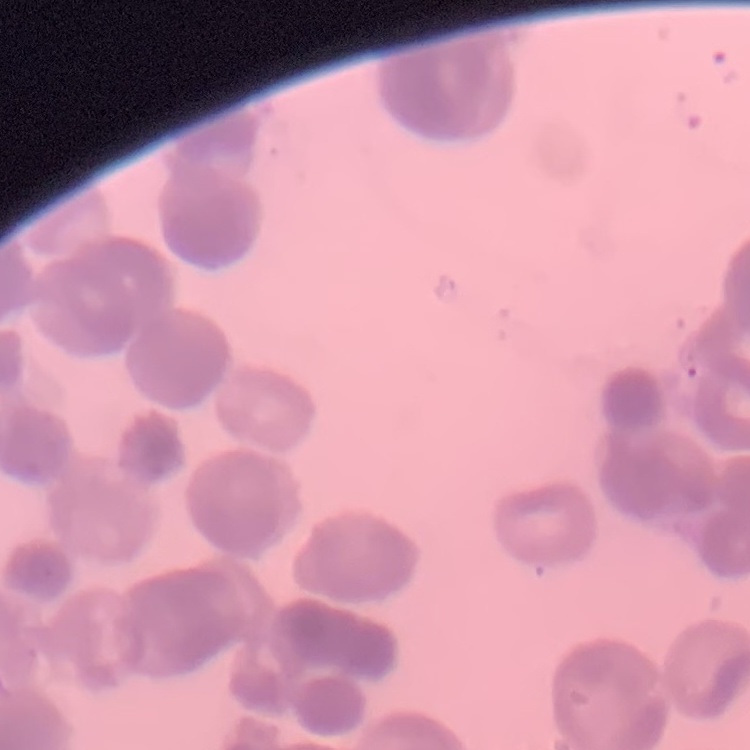

The red blood cells exhibit rouleaux formation. Square crop of a larger photomicrograph. Thin peripheral smear. Field's or Giemsa stain.